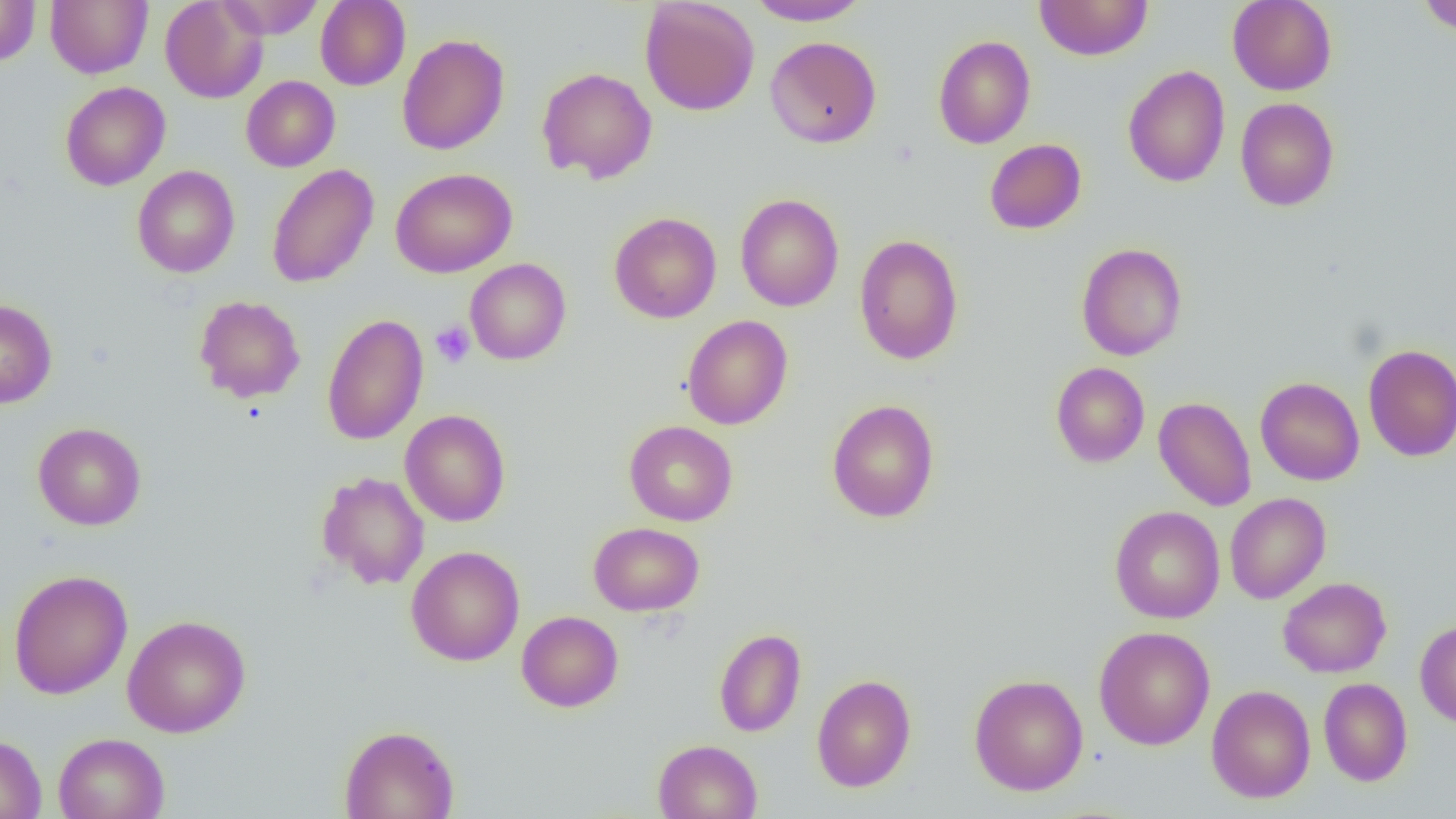
Approximate bounding boxes as (x1,y1)-(x2,y2) corner pairs in pixels. Platelet locations: (430,321)-(475,368). Uninfected red blood cell locations: (0,0)-(40,66), (46,0)-(151,78), (159,0)-(268,103), (217,0)-(324,39), (316,0)-(411,90), (640,0)-(760,116), (746,0)-(872,25), (1034,0)-(1153,61), (1227,0)-(1337,95), (1417,0)-(1456,35), (396,33)-(510,155), (933,35)-(1036,149), (765,36)-(882,148), (1123,65)-(1230,188), (537,67)-(657,184), (241,75)-(340,172), (60,81)-(170,190), (1235,97)-(1340,211), (984,139)-(1086,235), (266,164)-(379,288), (132,165)-(240,278), (391,168)-(518,278), (735,194)-(844,312), (609,212)-(722,323), (854,233)-(964,365), (1076,242)-(1188,360), (465,258)-(572,365), (193,295)-(306,403), (0,299)-(57,409), (321,314)-(429,445), (682,315)-(793,430), (1363,343)-(1456,461), (1050,362)-(1150,467), (1255,377)-(1364,485), (1153,396)-(1257,511), (826,398)-(940,523), (399,409)-(511,527), (624,420)-(738,526), (33,422)-(146,530), (316,471)-(430,590), (1225,493)-(1331,604), (1109,505)-(1225,623), (589,522)-(704,615), (406,545)-(525,666), (8,569)-(133,699), (1278,577)-(1391,678), (516,610)-(623,712), (121,614)-(251,738), (1415,619)-(1456,728), (1094,626)-(1215,750), (714,628)-(806,737), (969,673)-(1088,795), (811,674)-(916,792), (1318,677)-(1413,786), (1206,685)-(1316,803), (339,724)-(459,819), (53,732)-(170,819), (0,734)-(46,819), (653,739)-(762,819). Slide-level diagnosis: no evidence of blood parasites. Image is 1456×819 pixels. Thin blood film. Light microscopy. Single field of view. Captured at 1000x magnification.